Assess this cell for malaria.
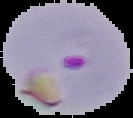

Parasitized.

{
  "preparation": "thin blood film",
  "image_type": "cell region segmented out of the field of view; surrounding area masked to black",
  "image_size": "133×118 pixels"
}